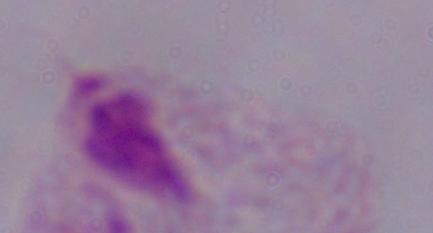

{
  "magnification": "1000x",
  "identification": "trichomonad",
  "modality": "micrograph"
}